Assess this cell for malaria.
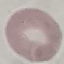
Uninfected.

Giemsa stain. Cell patch, automatically extracted from a larger field of view and resized to 64 × 64 pixels. Acquired by smartphone through the microscope eyepiece. Thin blood film.